Report the malaria status of this cell.
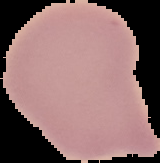
It is uninfected.

Image is 160×163 pixels. The area outside the segmented cell region is set to black. From a thin blood smear.